Name the cell type shown.
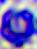

This is a leukocyte.

Summary:
  - Modality: photomicrograph
  - Magnification: 400x